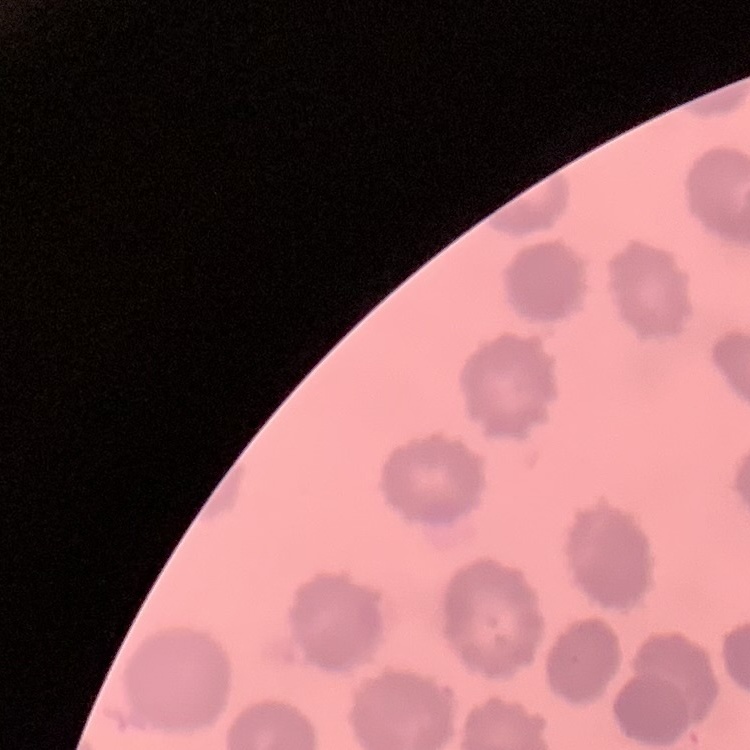

red blood cell morphology = no rouleaux formation
image type = square crop of a larger photomicrograph
preparation = thin blood smear
stain = Field's or Giemsa